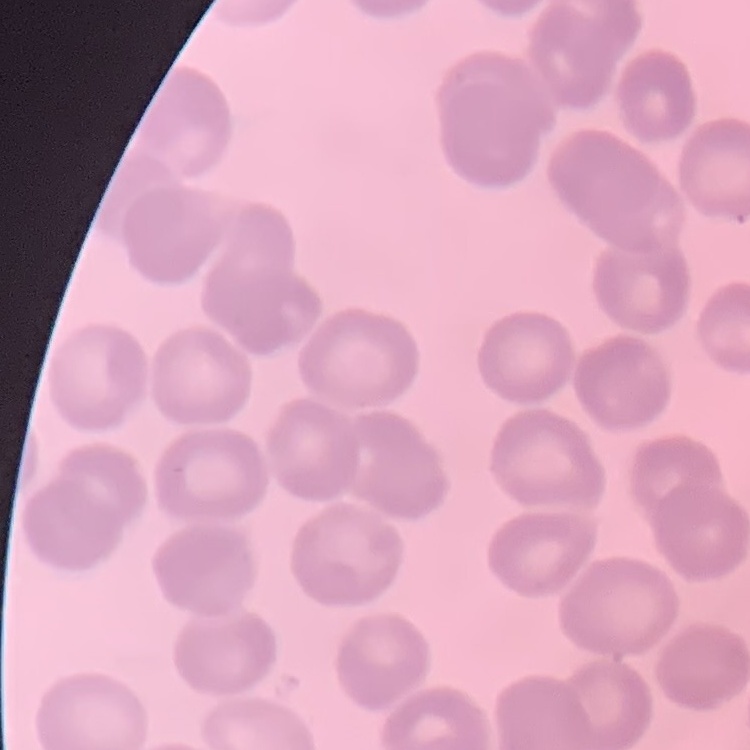

Summary:
  - Erythrocyte morphology: no rouleaux formation
  - Preparation: thin peripheral smear
  - Stain: Field's or Giemsa
  - Image type: square crop of a larger photomicrograph